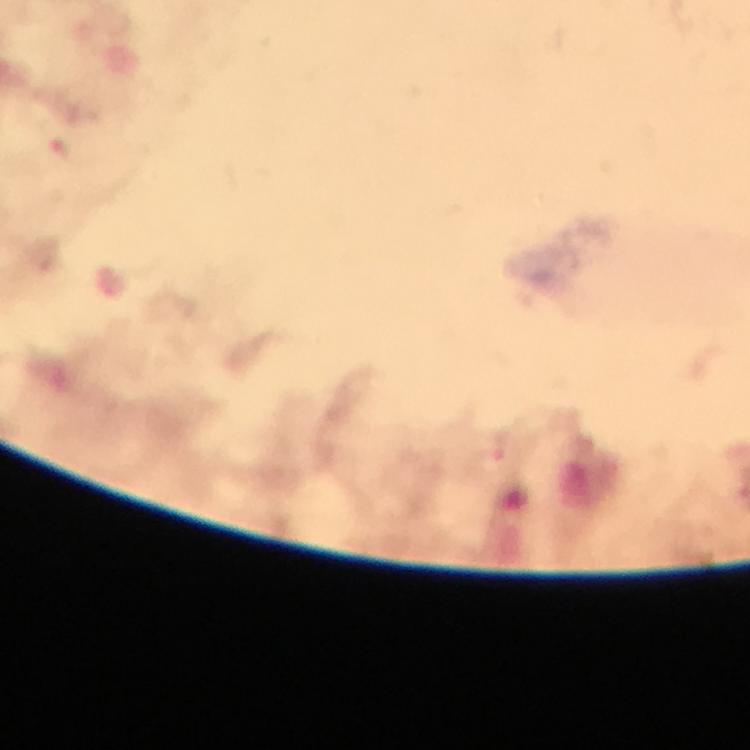

Approximate centers as (x, y) in pixels. Malaria parasite locations: (64, 152), (498, 458). Giemsa-stained preparation. Photographed with a smartphone mounted on the microscope. From a malaria diagnostic workup. Immersion oil was used. Image is 750×750 pixels. 100x magnification. A crop from one field of view. Thick blood smear.